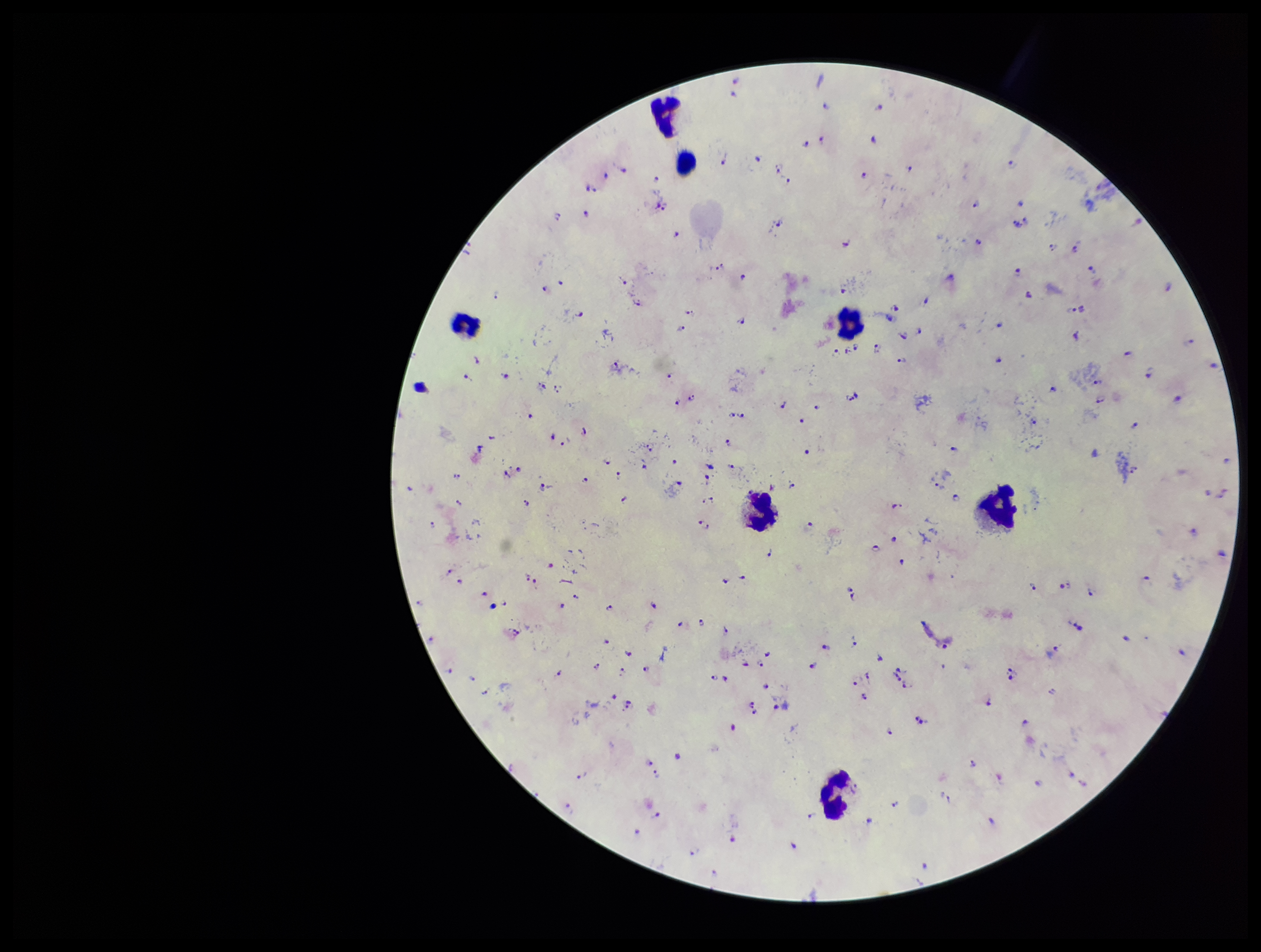
Summary:
  - Stain: Giemsa
  - Patient malaria status: infected
  - Field of view: single
  - Leukocyte count: 7
  - Capture: smartphone photograph through the microscope eyepiece
  - Species reported for this patient: Plasmodium falciparum
  - Parasite count: 173
  - Preparation: thick
  - Image size: 1261×952 pixels
  - Plasmodium parasites: identified